Assess the morphology of the erythrocytes.
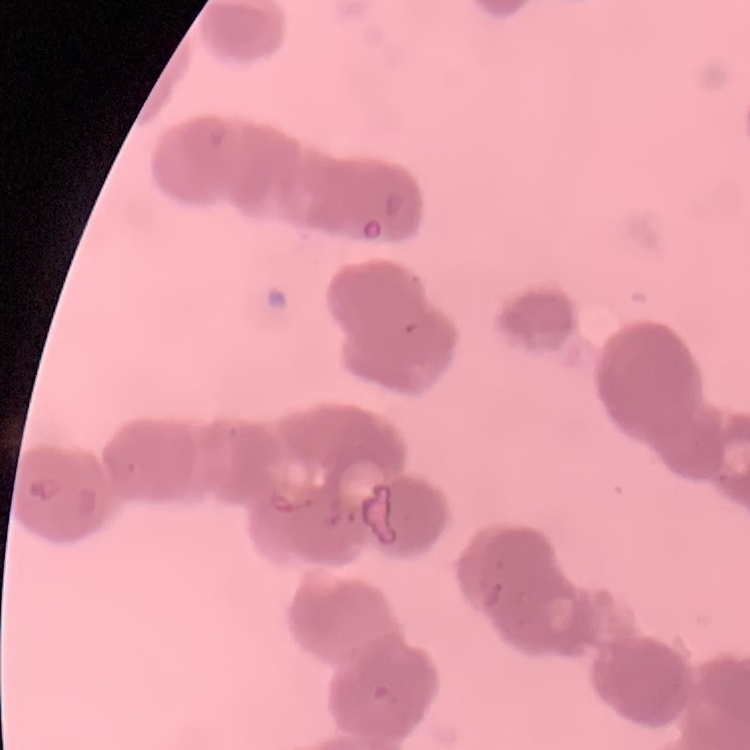

They show rouleaux formation.

Summary:
  - Image type: square crop of a larger photomicrograph
  - Stain: Field's or Giemsa
  - Preparation: thin blood film